Locate every uninfected red blood cell.
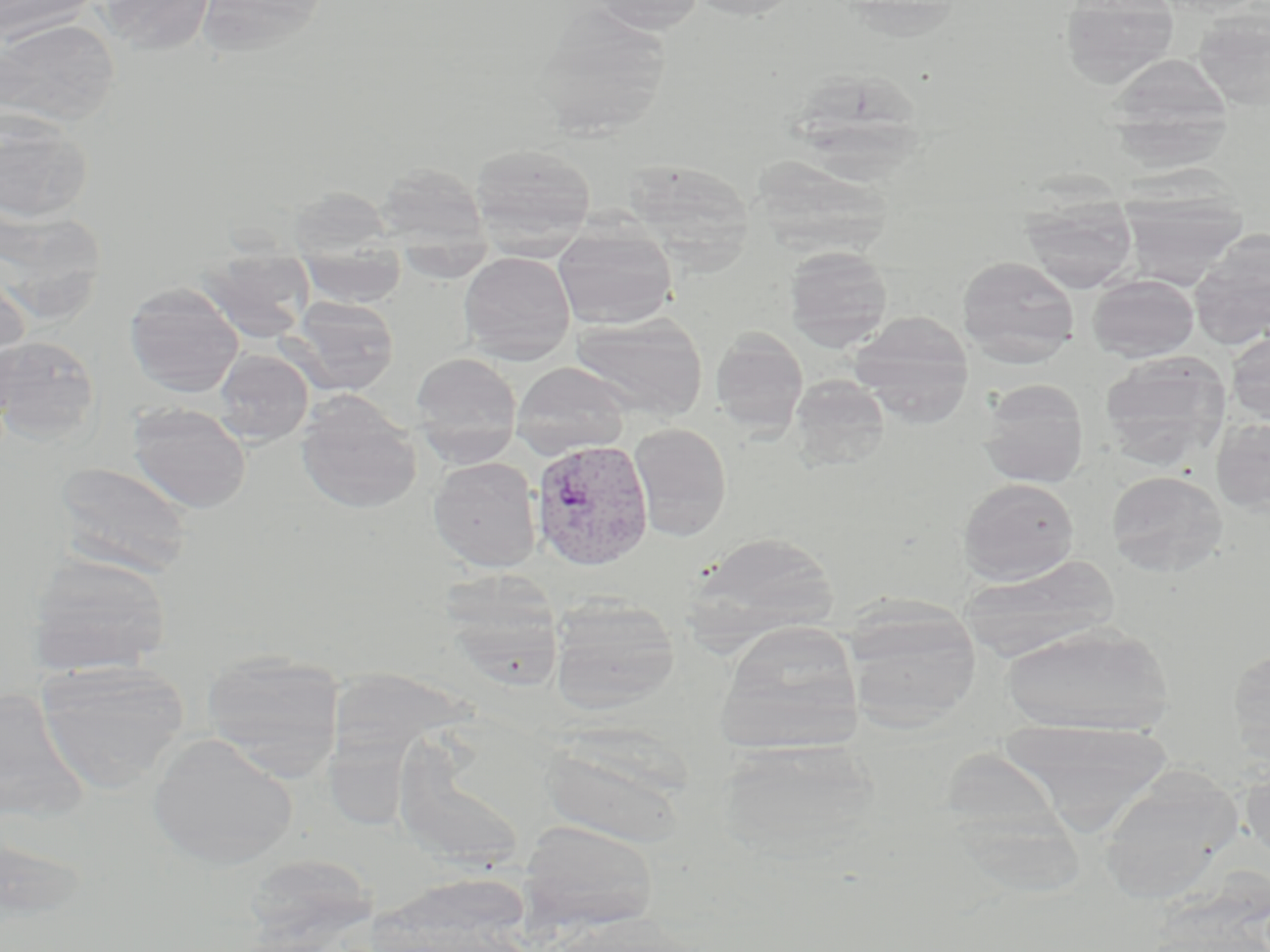

Approximate bounding boxes as (x1,y1)-(x2,y2) corner pairs in pixels.
Uninfected red blood cells: (0,0)-(100,44), (95,0)-(218,56), (196,0)-(330,59), (583,0)-(707,34), (684,0)-(807,21), (1060,0)-(1180,87), (528,8)-(674,138), (1193,8)-(1270,111), (0,18)-(120,129), (1110,53)-(1231,140), (801,74)-(933,187), (0,107)-(94,223), (1106,111)-(1232,175), (469,144)-(596,243), (751,154)-(894,255), (623,159)-(755,261), (374,163)-(489,250), (287,187)-(397,258), (1119,191)-(1248,287), (1022,196)-(1137,292), (0,201)-(107,324), (1189,231)-(1270,349), (553,234)-(677,328), (395,244)-(496,281), (784,246)-(893,350), (193,251)-(315,343), (459,251)-(576,364), (298,255)-(407,307), (957,255)-(1080,366), (0,266)-(31,390), (1087,274)-(1199,362), (124,282)-(244,397), (286,297)-(400,395), (571,312)-(708,421), (849,312)-(974,422), (710,329)-(809,435), (1226,332)-(1270,425), (0,334)-(101,444), (213,349)-(314,446), (410,353)-(521,455), (1100,353)-(1230,468), (511,362)-(631,457), (790,374)-(890,471), (977,379)-(1089,487), (294,393)-(424,515), (127,402)-(252,514), (1211,418)-(1270,514), (629,422)-(732,541), (428,457)-(542,572), (52,460)-(194,578), (1107,470)-(1228,576), (957,477)-(1079,584), (692,531)-(838,637), (26,552)-(173,677), (959,555)-(1120,662), (440,572)-(565,688), (549,596)-(680,716), (845,604)-(982,731), (714,619)-(866,752), (999,622)-(1175,736), (201,650)-(344,779), (1228,650)-(1270,760), (35,660)-(190,793), (332,668)-(472,829), (0,688)-(86,824), (999,720)-(1176,835), (148,733)-(297,870), (539,735)-(691,848), (718,738)-(883,862), (1240,761)-(1270,864), (1098,765)-(1241,904), (519,820)-(659,932), (254,852)-(374,950).

Summary:
  - Plasmodium vivax-infected red blood cell locations: (530,438)-(654,571)
  - Slide-level diagnosis: Plasmodium vivax
  - Preparation: thin blood smear
  - Stain: May-Grünwald-Giemsa
  - Magnification: 1000x
  - Field of view: one of a larger specimen
  - Modality: optical microscopy
  - Image size: 1270×952 pixels